Assess this cell for malaria.
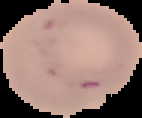

Uninfected.

From a thin blood film. Image is 142×118 pixels. The area outside the segmented cell region is set to black.